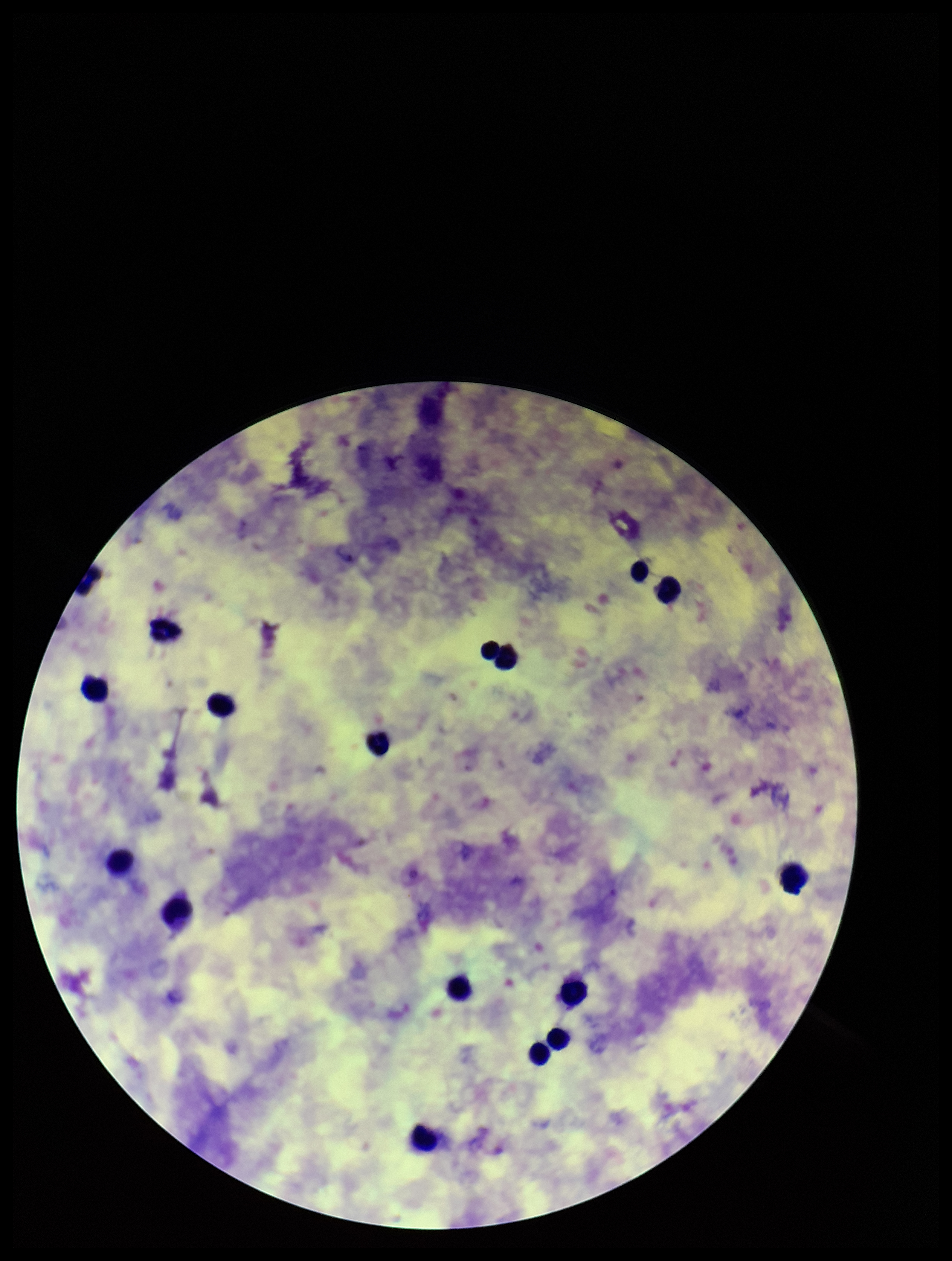
field of view = single
Plasmodium parasites = none seen
image size = 952×1261 pixels
stain = Giemsa
species reported for this patient = Plasmodium falciparum
capture = smartphone photograph through the microscope eyepiece
parasite count = 0
leukocyte count = 14
patient malaria status = positive
preparation = thick smear